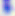

400x magnification. Micrograph. Toxoplasma gondii is shown.